Assess this cell for malaria.
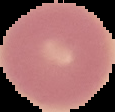

It is uninfected.

image_size: 115×112 pixels
preparation: thin blood film
image_type: segmented cell region with the area outside set to black